Locate every blood parasite and identify its species.
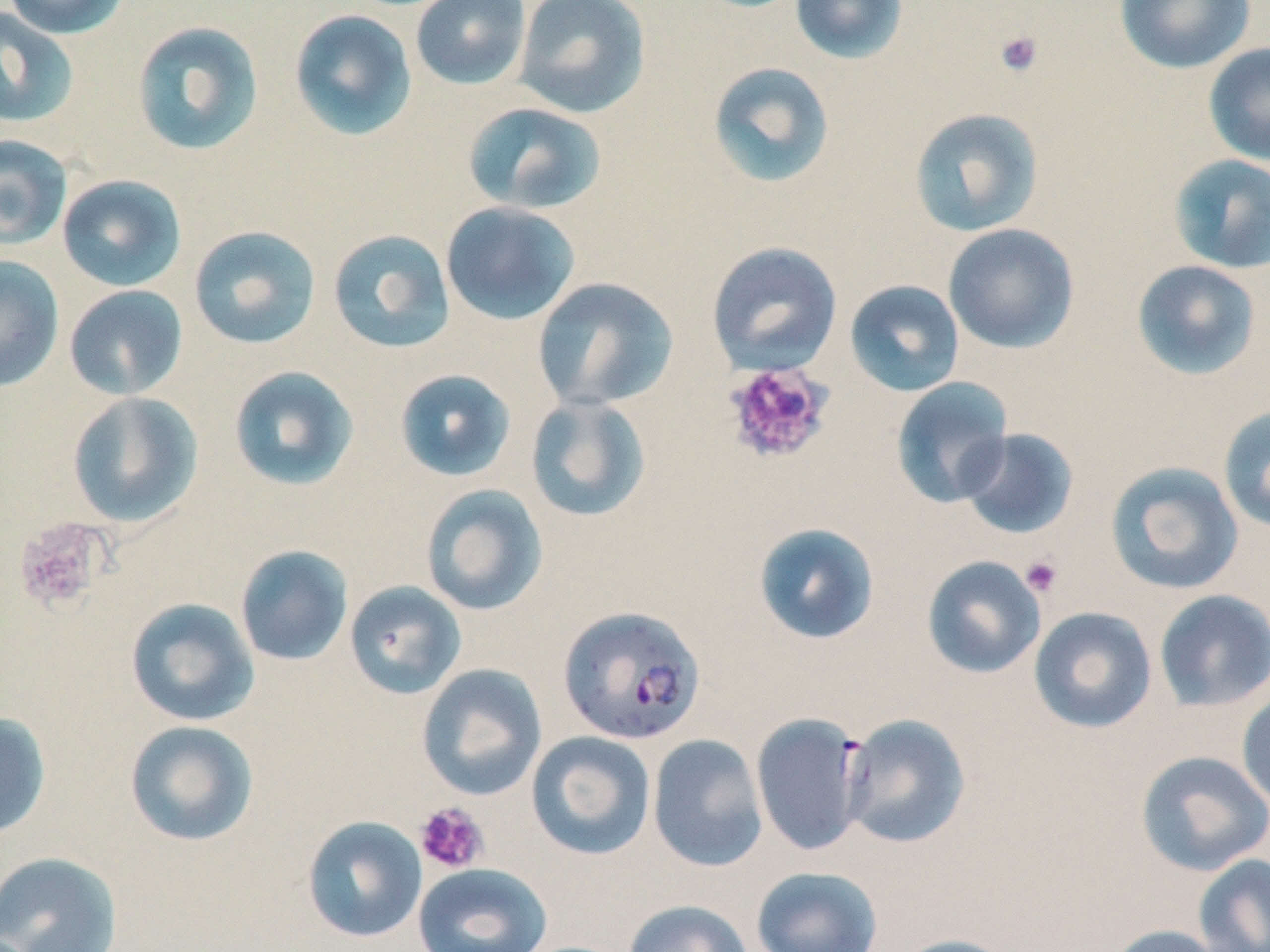
Approximate bounding boxes as [x1, y1, x2, y2] in pixels.
Plasmodium falciparum-infected red blood cells: [557, 604, 705, 746].
No Plasmodium ovale, Plasmodium malariae, Plasmodium vivax, Babesia divergens, or Trypanosoma brucei observed.

slide-level diagnosis = Plasmodium falciparum
uninfected red blood cell locations = approximate bounding boxes as [x1, y1, x2, y2] in pixels: [2, 0, 131, 39], [410, 0, 532, 91], [513, 0, 651, 119], [789, 0, 909, 65], [1114, 0, 1256, 74], [0, 7, 79, 128], [288, 9, 418, 142], [131, 21, 265, 156], [1203, 42, 1270, 166], [706, 61, 835, 189], [462, 102, 607, 215], [909, 108, 1044, 237], [0, 135, 72, 251], [1168, 154, 1270, 274], [57, 175, 187, 292], [440, 201, 581, 326], [943, 223, 1080, 353], [189, 225, 321, 349], [327, 228, 456, 354], [706, 241, 843, 375], [0, 255, 64, 393], [1131, 259, 1264, 381], [531, 276, 679, 411], [844, 280, 965, 397], [64, 285, 188, 400], [228, 365, 360, 491], [394, 369, 517, 482], [890, 376, 1014, 508], [66, 391, 204, 528], [525, 395, 652, 523], [1218, 404, 1270, 534], [957, 427, 1079, 540], [1105, 461, 1244, 595], [419, 484, 548, 616], [753, 522, 880, 645], [235, 545, 353, 666], [921, 555, 1047, 679], [343, 581, 467, 699], [1154, 590, 1270, 712], [125, 597, 259, 727], [1028, 606, 1157, 734], [416, 663, 547, 801], [1236, 691, 1270, 811], [0, 711, 51, 840], [750, 713, 870, 856], [839, 713, 971, 849], [124, 719, 260, 847], [526, 731, 657, 860], [647, 734, 768, 872], [1135, 749, 1270, 877], [302, 815, 427, 943], [0, 851, 123, 952], [1193, 853, 1270, 952], [412, 862, 553, 952], [750, 866, 883, 952], [623, 899, 754, 952], [1103, 924, 1228, 952], [890, 934, 1021, 952]
field of view = single
image size = 1270×952 pixels
modality = optical microscopy
platelet locations = approximate bounding boxes as [x1, y1, x2, y2] in pixels: [993, 29, 1044, 77], [721, 361, 834, 466], [13, 517, 109, 613], [1019, 555, 1063, 598], [413, 802, 489, 874]
stain = May-Grünwald-Giemsa
preparation = thin blood film
magnification = 1000x